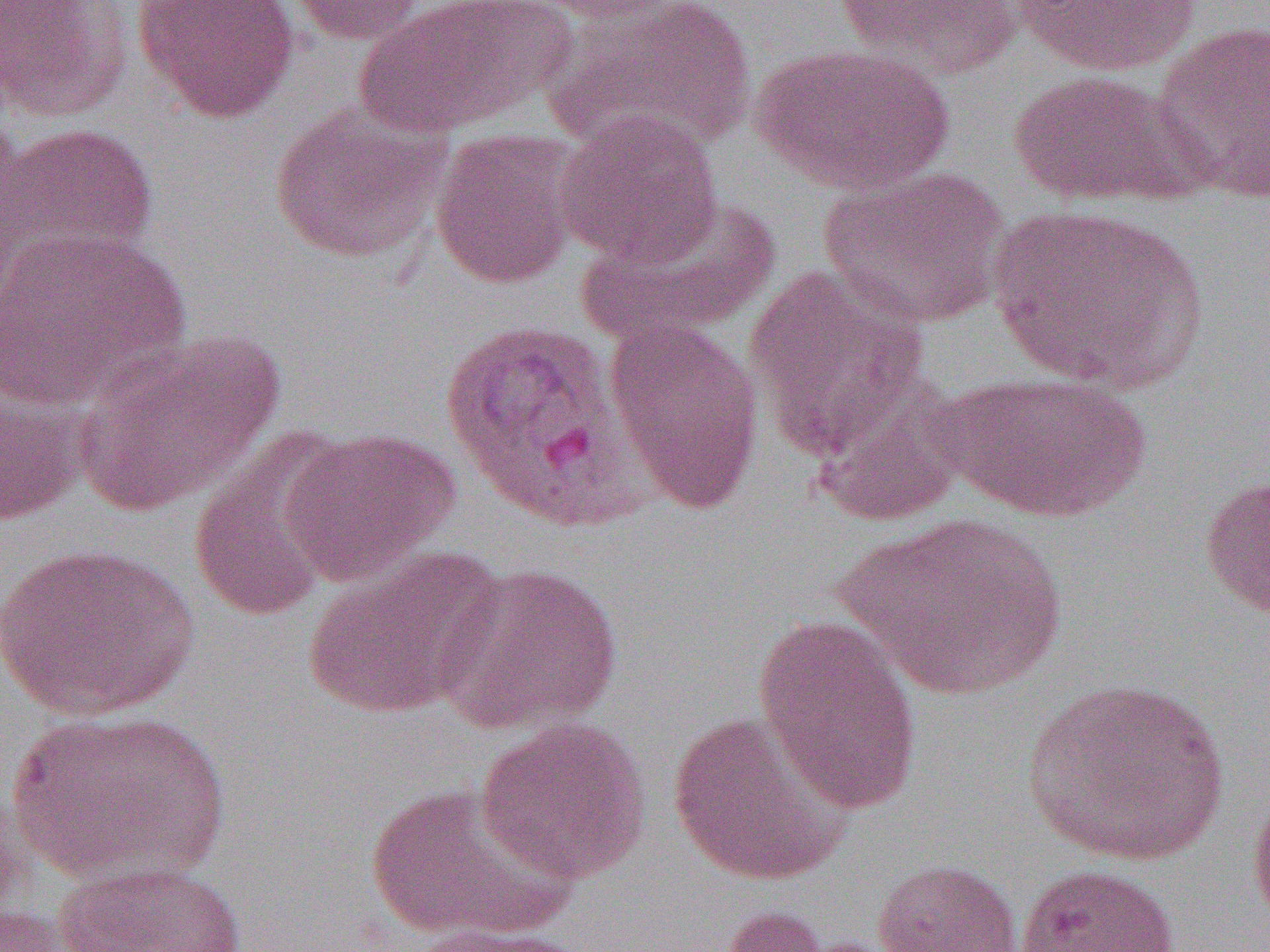

slide-level diagnosis = Plasmodium vivax
modality = optical microscopy
uninfected red blood cell locations = approximate bounding boxes as (x1, y1, x2, y2) in pixels: (0, 0, 135, 121), (132, 0, 301, 123), (285, 0, 434, 45), (352, 0, 563, 138), (529, 0, 690, 23), (543, 0, 757, 156), (833, 0, 1024, 79), (1010, 1, 1202, 77), (1150, 21, 1270, 202), (750, 44, 954, 195), (1008, 69, 1189, 206), (270, 103, 449, 264), (555, 109, 722, 266), (0, 121, 158, 286), (430, 130, 580, 289), (817, 165, 1011, 330), (580, 194, 783, 344), (989, 204, 1208, 392), (0, 227, 191, 410), (744, 264, 929, 455), (603, 317, 765, 516), (73, 328, 285, 516), (934, 371, 1152, 522), (808, 373, 969, 528), (0, 378, 88, 528), (188, 426, 351, 623), (283, 429, 458, 584), (1199, 472, 1270, 622), (841, 512, 1068, 699), (2, 541, 200, 721), (302, 546, 506, 720), (436, 560, 622, 735), (753, 613, 923, 813), (1021, 678, 1231, 866), (6, 706, 232, 885), (666, 710, 854, 887), (476, 715, 651, 885), (0, 773, 30, 922), (365, 780, 573, 944), (1247, 786, 1270, 936), (871, 858, 1024, 951), (55, 861, 250, 952), (1015, 863, 1178, 952), (0, 902, 93, 951), (716, 904, 841, 952), (402, 923, 587, 952)
preparation = thin blood smear
field of view = one of a larger specimen
magnification = 1000x
image size = 1270×952 pixels